Classify this cell by malaria status.
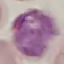

It is parasitized.

Automatically extracted cell patch, resized to 64 × 64 pixels. Giemsa-stained preparation. Photographed with a smartphone camera at the microscope eyepiece. Thin blood film.